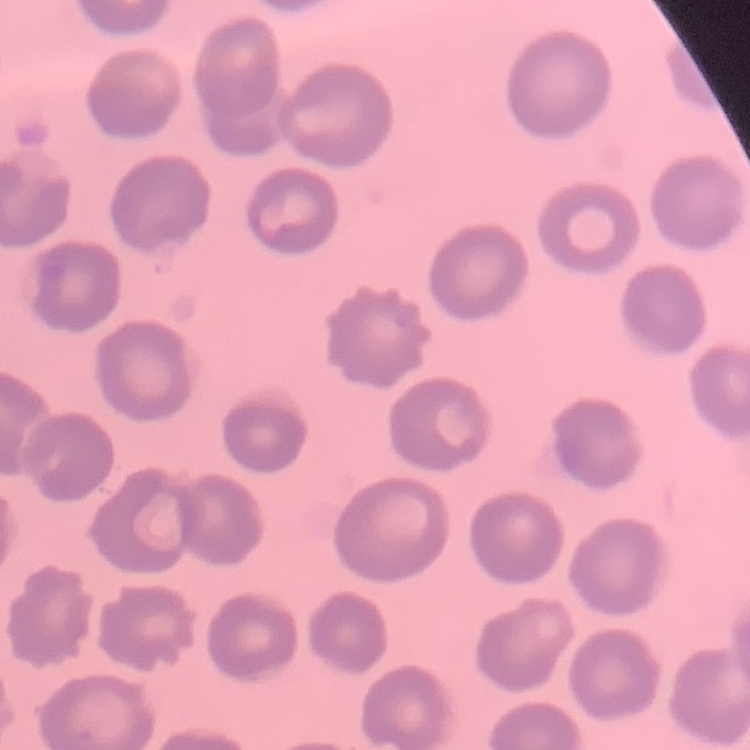
The red blood cells show no rouleaux formation. Thin blood smear. One tile cut from a larger photomicrograph. Field's or Giemsa stain.